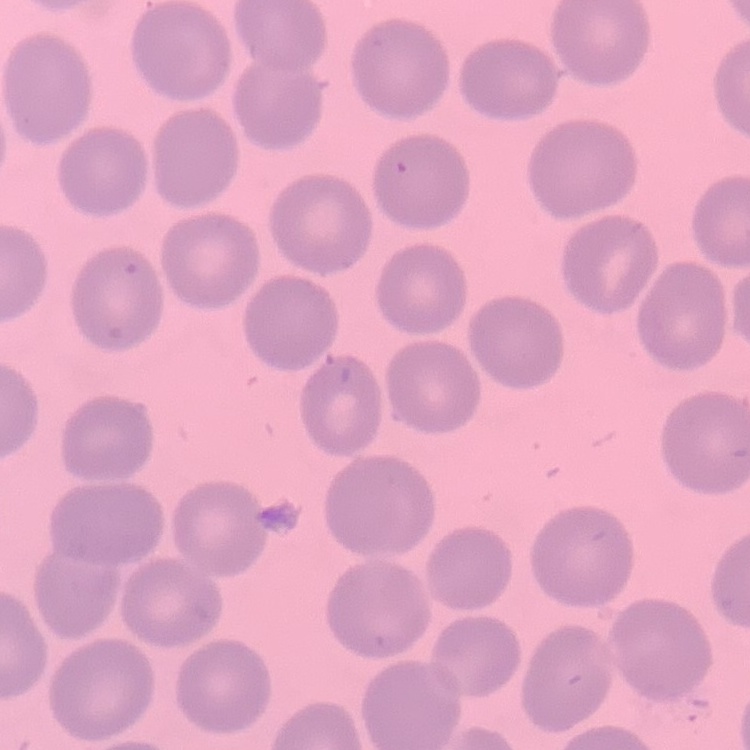
Summary:
  - Red blood cell morphology: no rouleaux formation
  - Preparation: thin peripheral smear
  - Image type: one tile cut from a larger photomicrograph
  - Stain: Field's or Giemsa